Assess this cell for malaria.
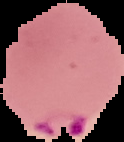

It is parasitized.

Summary:
  - Image type: segmented cell region on a black background
  - Preparation: thin blood film
  - Image size: 124×142 pixels